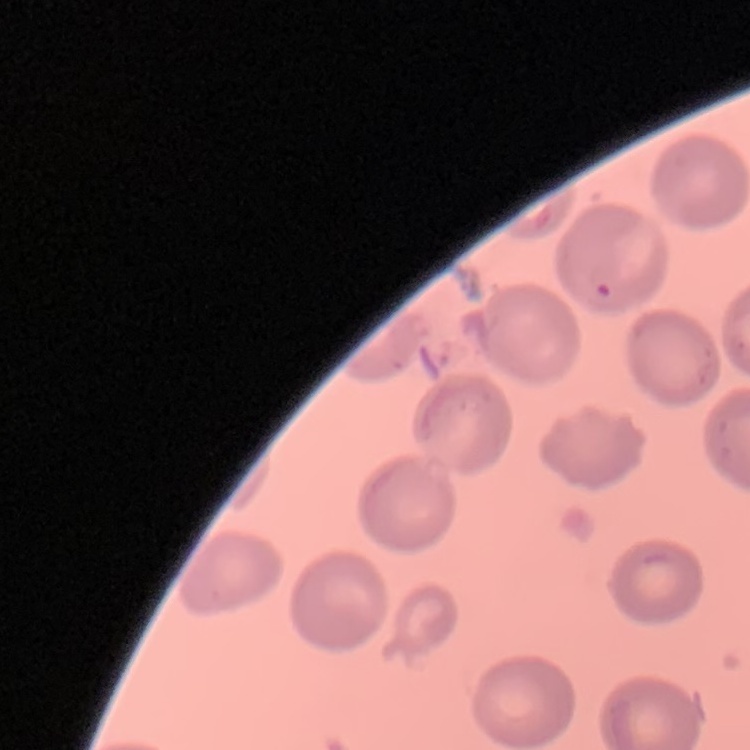
erythrocyte morphology = no rouleaux formation
image type = one tile cut from a larger photomicrograph
stain = Field's or Giemsa
preparation = thin peripheral smear